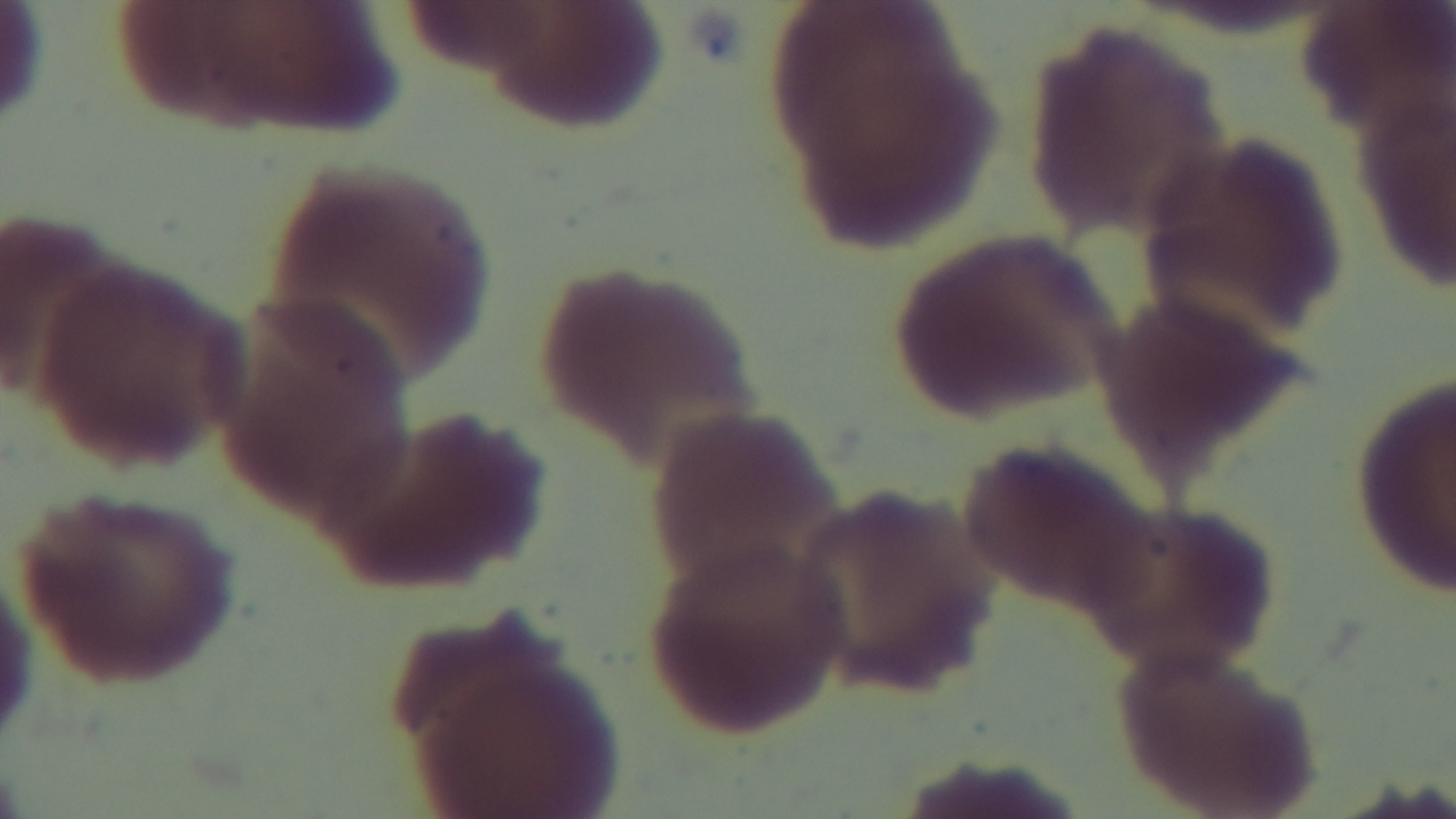
Summary:
  - Field of view: one from the slide
  - Modality: light microscopy
  - Capture: mounted 4K digital camera
  - Stain: Giemsa
  - Objective: 100x oil immersion
  - Preparation: thin blood film
  - Malaria status: negative